Locate and identify every blood parasite.
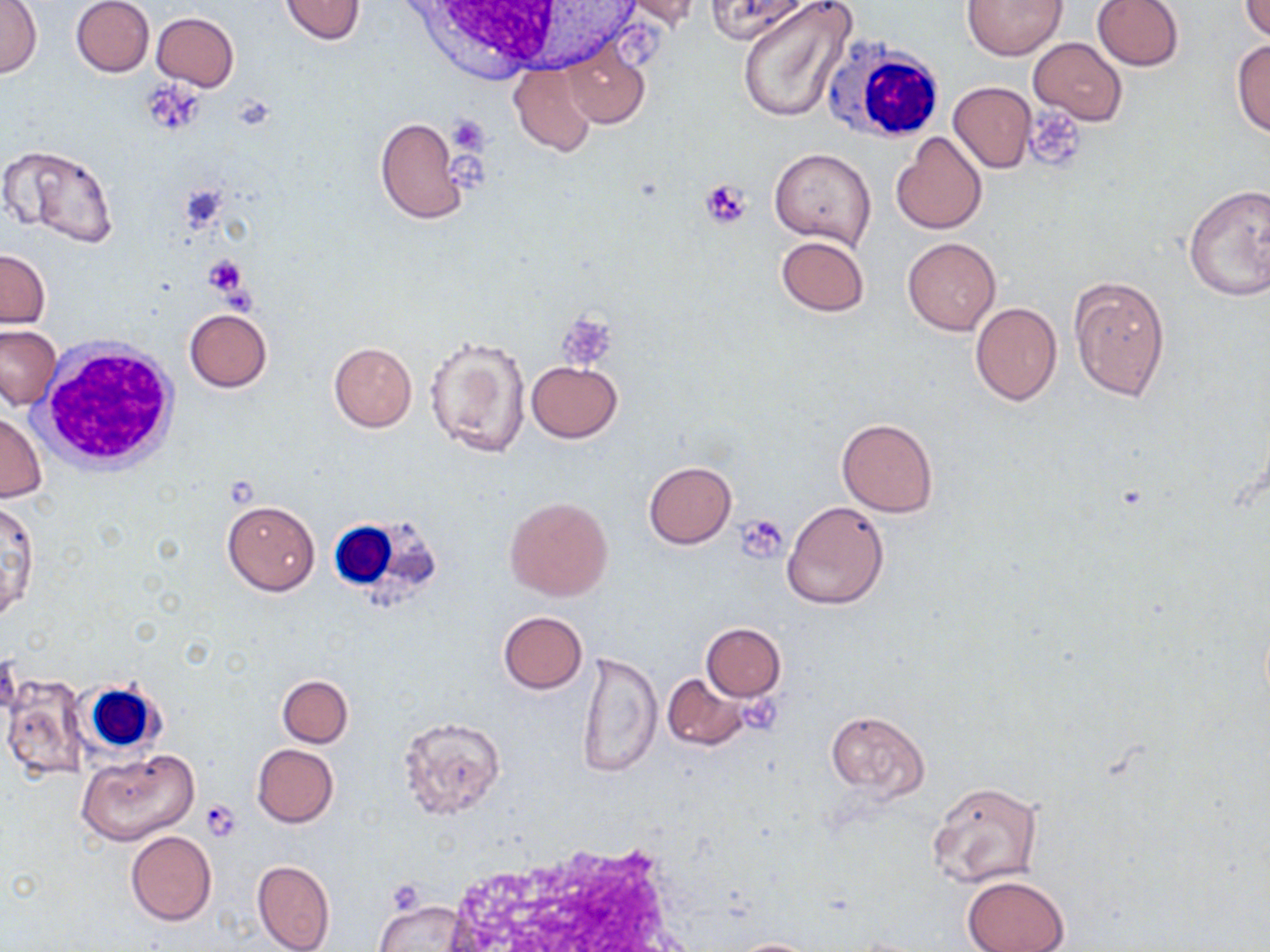
No blood parasites seen.

Approximate bounding boxes as named x1/y1/x2/y2 corners in pixels. White blood cell locations: (x1=381, y1=0, x2=619, y2=83), (x1=821, y1=38, x2=947, y2=145), (x1=35, y1=342, x2=181, y2=473), (x1=332, y1=510, x2=444, y2=604), (x1=77, y1=678, x2=164, y2=756). Uninfected red blood cell locations: (x1=72, y1=0, x2=154, y2=77), (x1=280, y1=0, x2=365, y2=47), (x1=612, y1=0, x2=704, y2=30), (x1=707, y1=0, x2=811, y2=42), (x1=734, y1=0, x2=857, y2=124), (x1=962, y1=0, x2=1066, y2=59), (x1=1092, y1=0, x2=1185, y2=71), (x1=0, y1=1, x2=40, y2=78), (x1=1240, y1=1, x2=1270, y2=40), (x1=152, y1=12, x2=239, y2=91), (x1=1029, y1=38, x2=1126, y2=125), (x1=561, y1=39, x2=650, y2=129), (x1=1233, y1=39, x2=1270, y2=138), (x1=508, y1=63, x2=597, y2=157), (x1=947, y1=82, x2=1036, y2=172), (x1=374, y1=115, x2=467, y2=226), (x1=890, y1=130, x2=987, y2=234), (x1=1, y1=144, x2=120, y2=246), (x1=770, y1=146, x2=876, y2=248), (x1=1182, y1=183, x2=1270, y2=300), (x1=775, y1=236, x2=869, y2=316), (x1=903, y1=238, x2=1000, y2=334), (x1=0, y1=249, x2=50, y2=328), (x1=1069, y1=275, x2=1169, y2=404), (x1=970, y1=301, x2=1062, y2=405), (x1=185, y1=309, x2=271, y2=391), (x1=0, y1=326, x2=60, y2=409), (x1=424, y1=333, x2=531, y2=460), (x1=328, y1=342, x2=417, y2=431), (x1=526, y1=361, x2=622, y2=442), (x1=1, y1=411, x2=47, y2=504), (x1=836, y1=418, x2=938, y2=517), (x1=643, y1=461, x2=736, y2=548), (x1=505, y1=496, x2=614, y2=602), (x1=222, y1=499, x2=320, y2=595), (x1=1, y1=500, x2=38, y2=622), (x1=781, y1=500, x2=889, y2=609), (x1=499, y1=611, x2=587, y2=693), (x1=700, y1=623, x2=785, y2=700), (x1=576, y1=649, x2=662, y2=780), (x1=662, y1=672, x2=752, y2=750), (x1=3, y1=675, x2=89, y2=784), (x1=277, y1=675, x2=352, y2=746), (x1=825, y1=708, x2=931, y2=802), (x1=399, y1=717, x2=505, y2=818), (x1=252, y1=744, x2=338, y2=827), (x1=76, y1=748, x2=199, y2=846), (x1=926, y1=780, x2=1042, y2=888), (x1=126, y1=831, x2=216, y2=925), (x1=251, y1=859, x2=335, y2=952), (x1=962, y1=875, x2=1070, y2=952), (x1=374, y1=899, x2=470, y2=951), (x1=730, y1=938, x2=818, y2=951). Platelet locations: (x1=143, y1=84, x2=207, y2=129), (x1=1022, y1=106, x2=1086, y2=172), (x1=446, y1=116, x2=491, y2=156), (x1=701, y1=179, x2=753, y2=229), (x1=203, y1=255, x2=247, y2=296), (x1=558, y1=313, x2=617, y2=370), (x1=736, y1=514, x2=786, y2=562), (x1=739, y1=695, x2=785, y2=735), (x1=199, y1=799, x2=242, y2=841), (x1=385, y1=879, x2=426, y2=914). Slide-level diagnosis: no evidence of blood parasites. One field of a larger specimen. 1000x magnification. Image is 1270×952 pixels. Thin blood film. May-Grünwald-Giemsa stain. Optical microscopy.